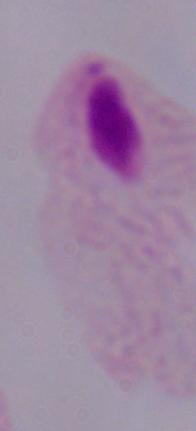
Photomicrograph. A trichomonad is seen. Captured at 1000x magnification.